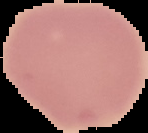
From a thin blood smear. Result: no malaria parasites detected. Cell region segmented out of the field of view; the surrounding area is masked to black. Image is 148×133 pixels.